State which parasite is depicted.
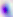
This is Toxoplasma gondii.

modality = photomicrograph
magnification = 400x